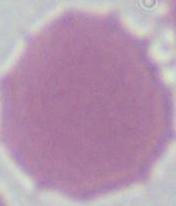
identification = red blood cell
modality = micrograph
magnification = 1000x